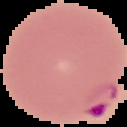

image type = cell region segmented out of the field of view; surrounding area masked to black
preparation = thin blood smear
image size = 127×127 pixels
malaria status = parasitized